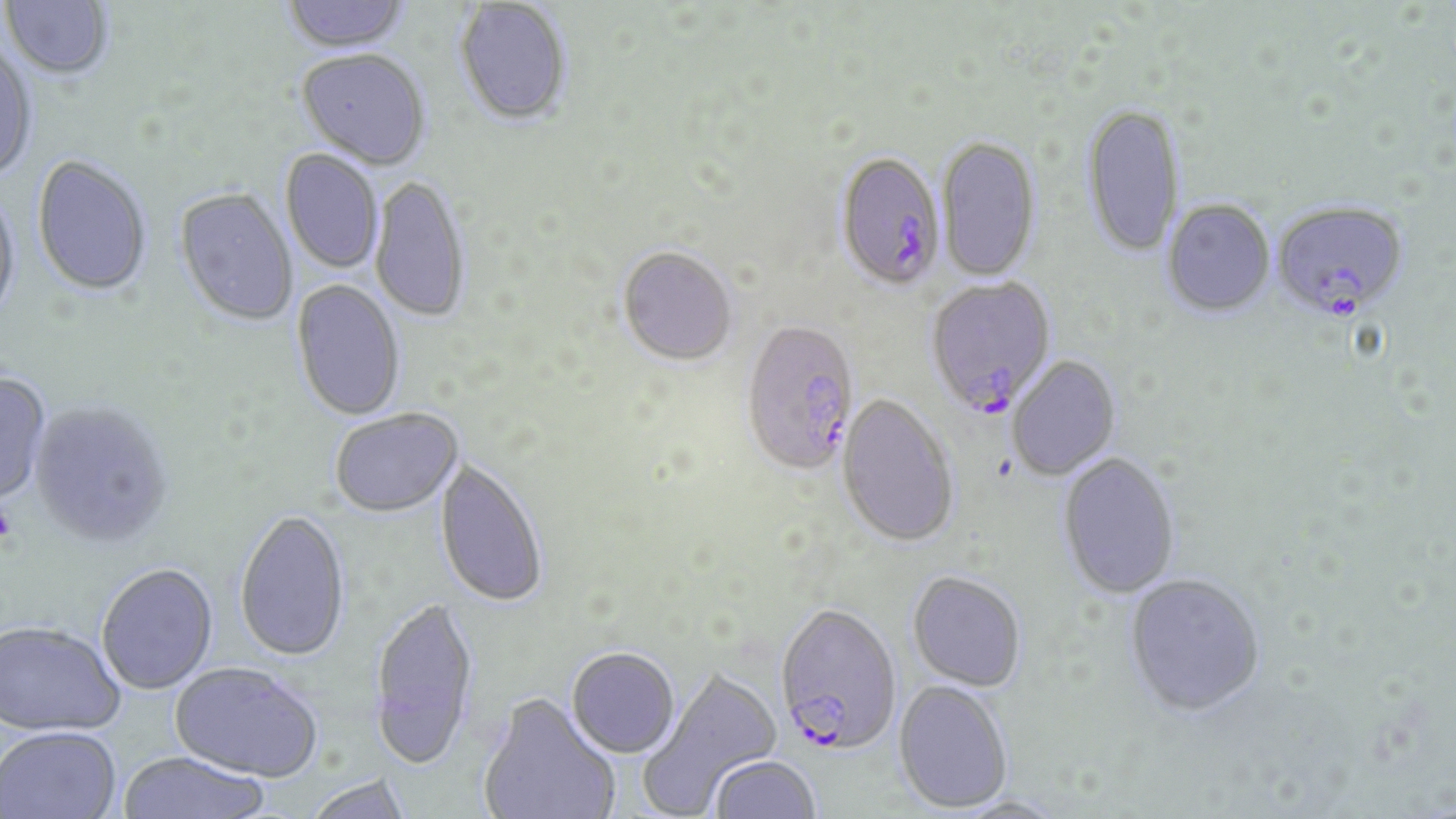

Approximate bounding boxes as (x1, y1, x2, y2) in pixels. Uninfected red blood cell locations: (2, 0, 113, 82), (281, 0, 412, 55), (454, 1, 573, 129), (0, 45, 38, 184), (296, 51, 431, 172), (1080, 105, 1185, 260), (937, 137, 1041, 283), (279, 150, 383, 274), (32, 157, 152, 298), (370, 176, 471, 323), (0, 188, 22, 327), (175, 190, 298, 328), (1162, 201, 1275, 319), (618, 248, 737, 367), (291, 279, 405, 422), (1006, 356, 1121, 481), (0, 371, 51, 505), (836, 395, 959, 549), (29, 401, 173, 549), (329, 410, 464, 519), (1057, 453, 1181, 600), (433, 459, 549, 610), (234, 510, 351, 664), (96, 564, 219, 695), (907, 572, 1027, 692), (1124, 575, 1266, 720), (368, 598, 479, 772), (1, 621, 126, 738), (566, 648, 680, 760), (170, 662, 323, 784), (639, 667, 783, 814), (893, 680, 1012, 813), (478, 696, 620, 819), (0, 726, 121, 819), (116, 752, 270, 819), (707, 756, 821, 818), (304, 775, 411, 819). Plasmodium falciparum-infected red blood cell locations: (834, 155, 947, 294), (1271, 201, 1410, 324), (924, 276, 1058, 419), (741, 323, 861, 478), (774, 604, 901, 756). Slide-level diagnosis: Plasmodium falciparum. May-Grünwald-Giemsa stain. Thin blood film. Captured at 1000x magnification. Single field of view. Optical microscopy. Image is 1456×819 pixels.